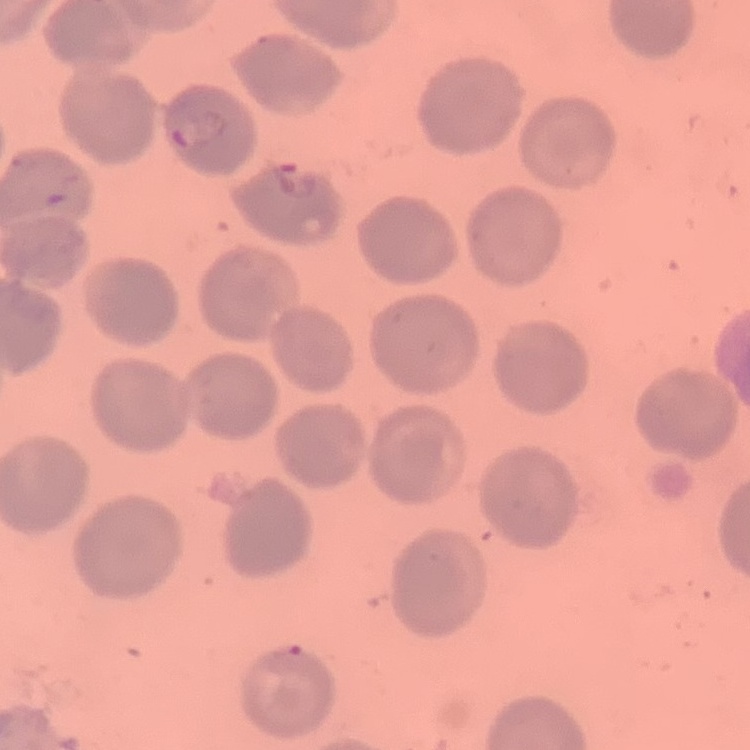
The erythrocytes show no rouleaux formation. Stained with either Field's or Giemsa. Thin peripheral smear. One tile cut from a larger photomicrograph.